Assess the morphology of the erythrocytes.
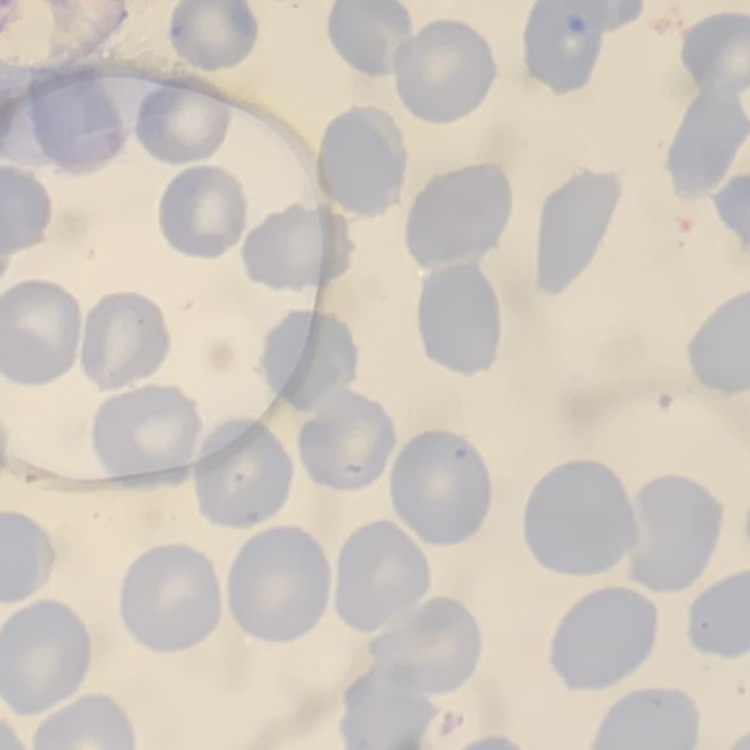
They show no rouleaux formation.

preparation = thin peripheral smear
image type = one tile cut from a larger photomicrograph
stain = Field's or Giemsa